Locate every Plasmodium parasite.
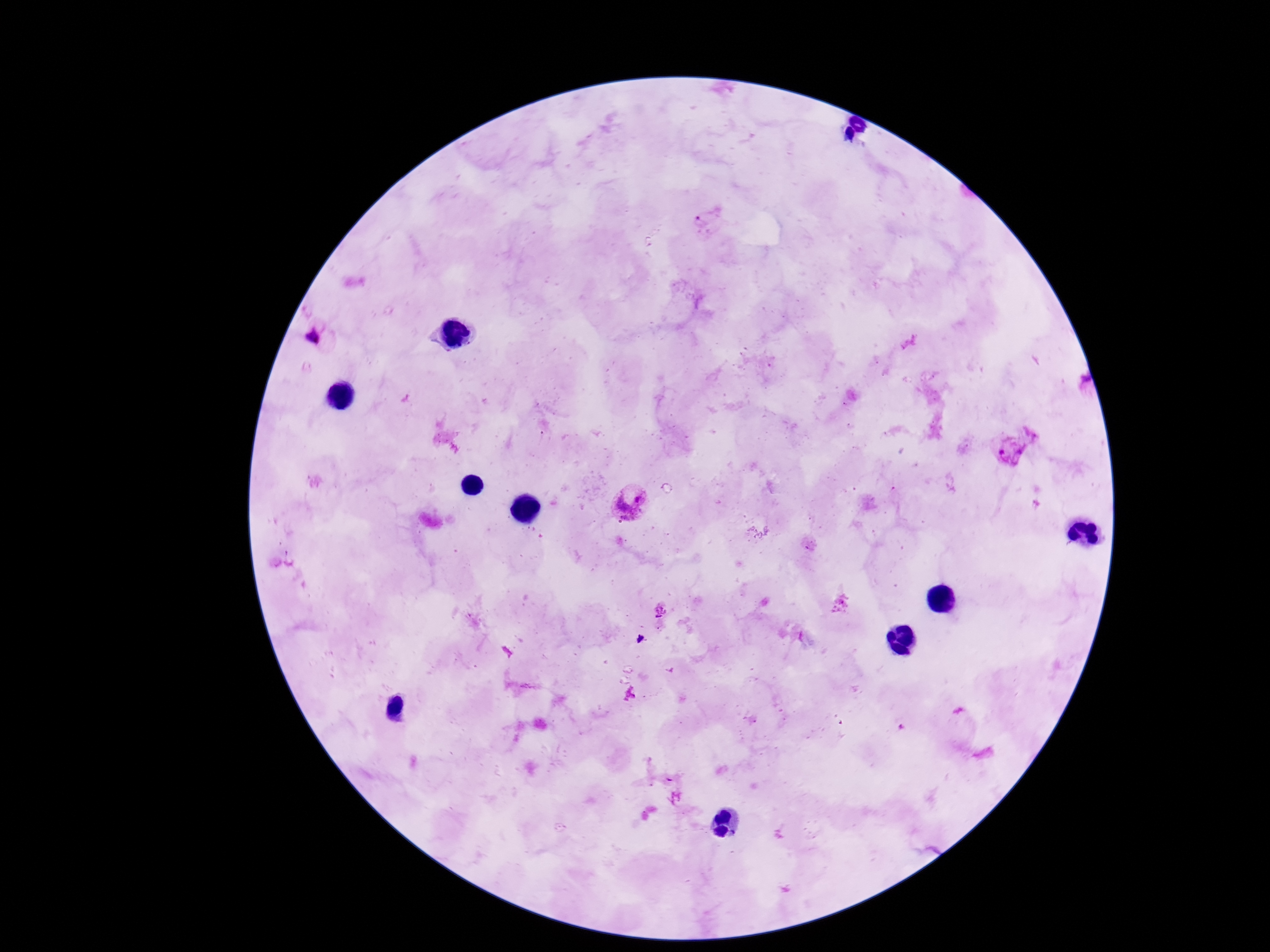
Approximate centers as [x, y] in pixels.
Plasmodium parasites: [708, 224], [312, 337], [1036, 430], [1010, 449], [632, 504], [660, 610], [661, 625], [641, 639].

100x magnification. Giemsa-stained preparation. Smartphone photograph taken through the microscope eyepiece. Thick blood smear. Image is 1270×952 pixels. Patient malaria status: positive. One field from this slide.